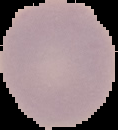

malaria status = uninfected
image size = 118×130 pixels
preparation = thin blood film
image type = cell region segmented out of the field of view; surrounding area masked to black